Give the extent of all Plasmodium parasites.
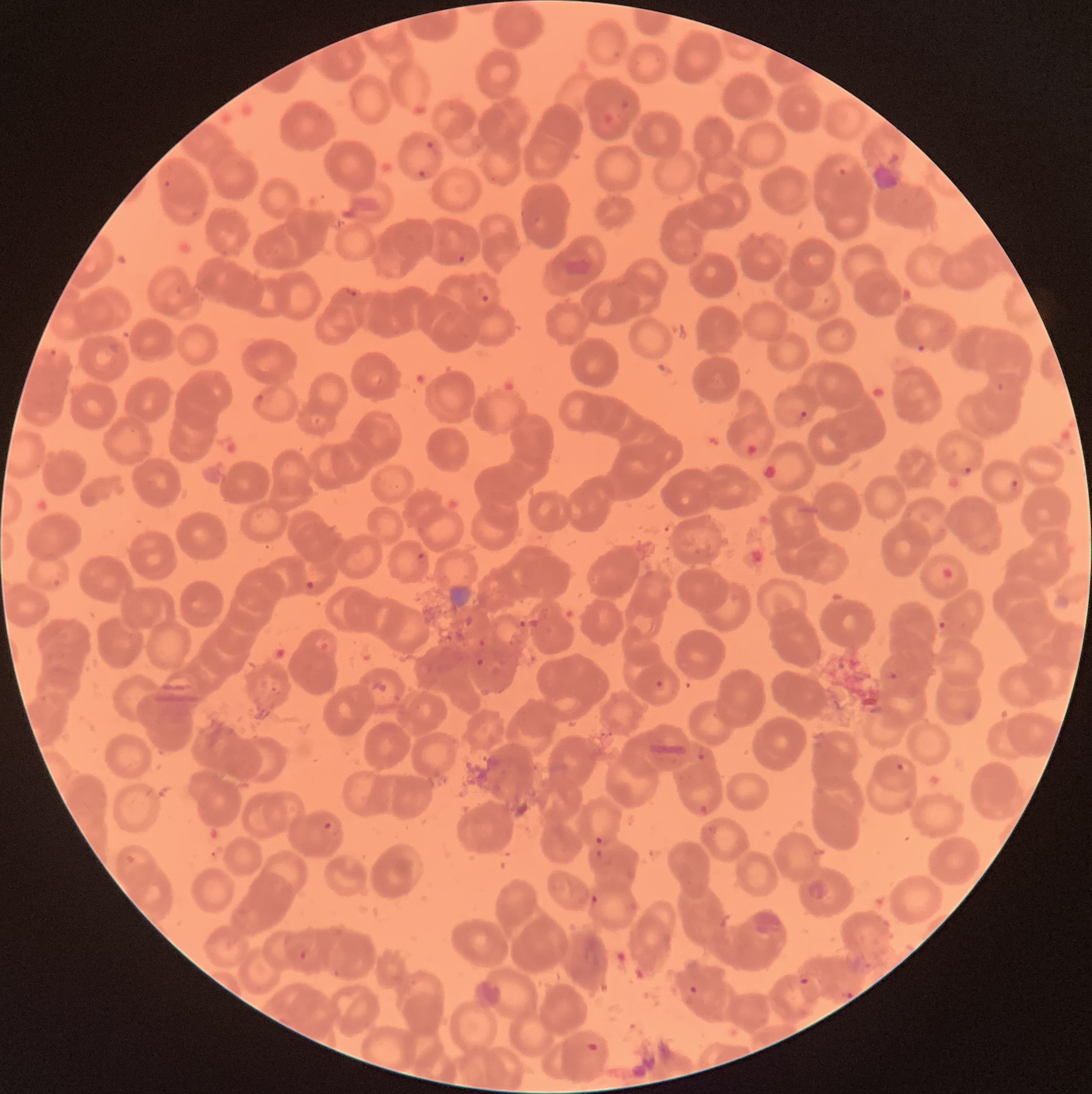

Approximate bounding boxes as (x1, y1, x2, y2) in pixels.
Plasmodium parasites: (619, 99, 631, 110), (604, 113, 616, 126), (424, 140, 437, 151), (833, 161, 854, 176), (417, 169, 429, 180), (163, 179, 173, 188), (188, 210, 198, 218), (690, 250, 700, 258), (457, 255, 467, 263), (343, 287, 363, 297), (479, 288, 493, 305), (107, 341, 120, 354), (48, 348, 67, 366), (255, 394, 266, 402), (800, 410, 808, 419), (961, 464, 974, 475), (1010, 478, 1021, 490), (417, 551, 429, 564), (52, 578, 62, 588), (304, 581, 315, 591), (518, 619, 527, 629), (939, 619, 950, 630), (473, 652, 484, 667), (884, 667, 899, 681), (653, 679, 664, 689), (693, 748, 706, 761), (895, 761, 909, 774), (322, 819, 334, 831), (707, 825, 720, 835), (593, 835, 605, 846), (590, 894, 600, 904), (299, 950, 306, 961), (798, 977, 812, 986), (688, 984, 699, 995), (842, 991, 854, 999), (586, 1042, 600, 1053).

Image is 1092×1094 pixels. Thin blood film. The red blood cells show rouleaux formation. Optical microscopy.